Classify this cell by malaria status.
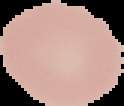
It is uninfected.

Summary:
  - Image size: 124×106 pixels
  - Preparation: thin blood smear
  - Image type: segmented cell region on a black background